Locate every blood parasite and identify its species.
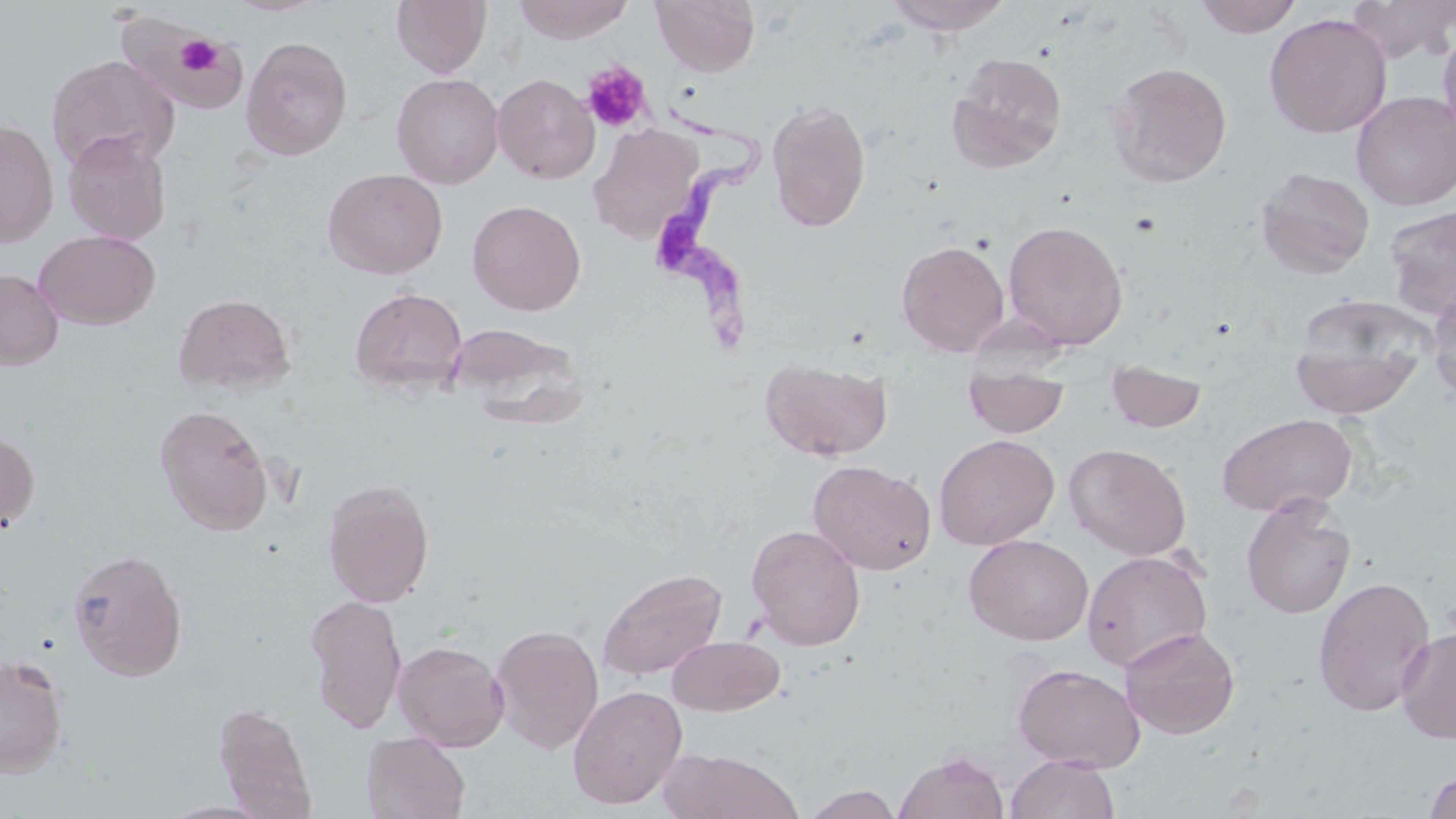

Approximate bounding boxes as (x1, y1, x2, y2) in pixels.
Trypanosoma brucei: (653, 93, 778, 352).
No Plasmodium falciparum, Plasmodium ovale, Plasmodium malariae, Plasmodium vivax, or Babesia divergens observed.

slide_level_diagnosis: Trypanosoma brucei
platelet_locations: 'approximate bounding boxes as (x1, y1, x2, y2) in pixels: (175, 36, 220, 77), (581, 61, 652, 133)'
stain: May-Grünwald-Giemsa
field_of_view: single
magnification: 1000x
preparation: thin blood film
modality: optical microscopy
image_size: 1456×819 pixels
uninfected_red_blood_cell_locations: 'approximate bounding boxes as (x1, y1, x2, y2) in pixels: (225, 0, 330, 16), (392, 0, 491, 78), (513, 0, 634, 44), (652, 0, 761, 77), (884, 0, 1014, 34), (1192, 0, 1305, 38), (1346, 0, 1456, 63), (1264, 13, 1392, 138), (114, 17, 256, 111), (1437, 23, 1456, 143), (241, 35, 353, 160), (947, 52, 1068, 174), (45, 54, 180, 171), (1106, 61, 1232, 188), (391, 72, 504, 189), (492, 73, 600, 184), (1351, 90, 1456, 210), (766, 98, 871, 233), (0, 119, 58, 247), (588, 123, 704, 244), (63, 131, 171, 245), (322, 167, 448, 279), (1255, 167, 1375, 279), (467, 199, 586, 316), (1383, 205, 1456, 320), (1002, 219, 1129, 350), (34, 230, 160, 330), (896, 239, 1010, 356), (0, 268, 64, 370), (349, 286, 468, 396), (1426, 290, 1456, 405), (172, 293, 295, 394), (1289, 304, 1430, 419), (447, 320, 588, 427), (760, 357, 893, 461), (1105, 359, 1207, 434), (963, 364, 1071, 438), (155, 403, 273, 535), (1217, 412, 1358, 516), (0, 429, 39, 532), (934, 434, 1060, 550), (1064, 443, 1192, 560), (807, 460, 935, 575), (322, 477, 435, 608), (1241, 496, 1356, 619), (746, 523, 866, 651), (964, 534, 1093, 646), (68, 548, 188, 682), (1081, 550, 1213, 672), (597, 566, 728, 682), (1313, 575, 1435, 717), (304, 594, 408, 733), (489, 622, 604, 754), (1119, 626, 1241, 740), (1396, 627, 1456, 744), (667, 635, 785, 716), (393, 640, 509, 751), (1, 654, 69, 777), (1012, 662, 1145, 772), (567, 685, 688, 809), (212, 701, 317, 816), (361, 732, 471, 819), (656, 748, 803, 819), (895, 751, 1009, 819), (1004, 753, 1120, 819), (1423, 771, 1456, 818), (801, 784, 903, 819)'